Give the position of every Plasmodium parasite visible.
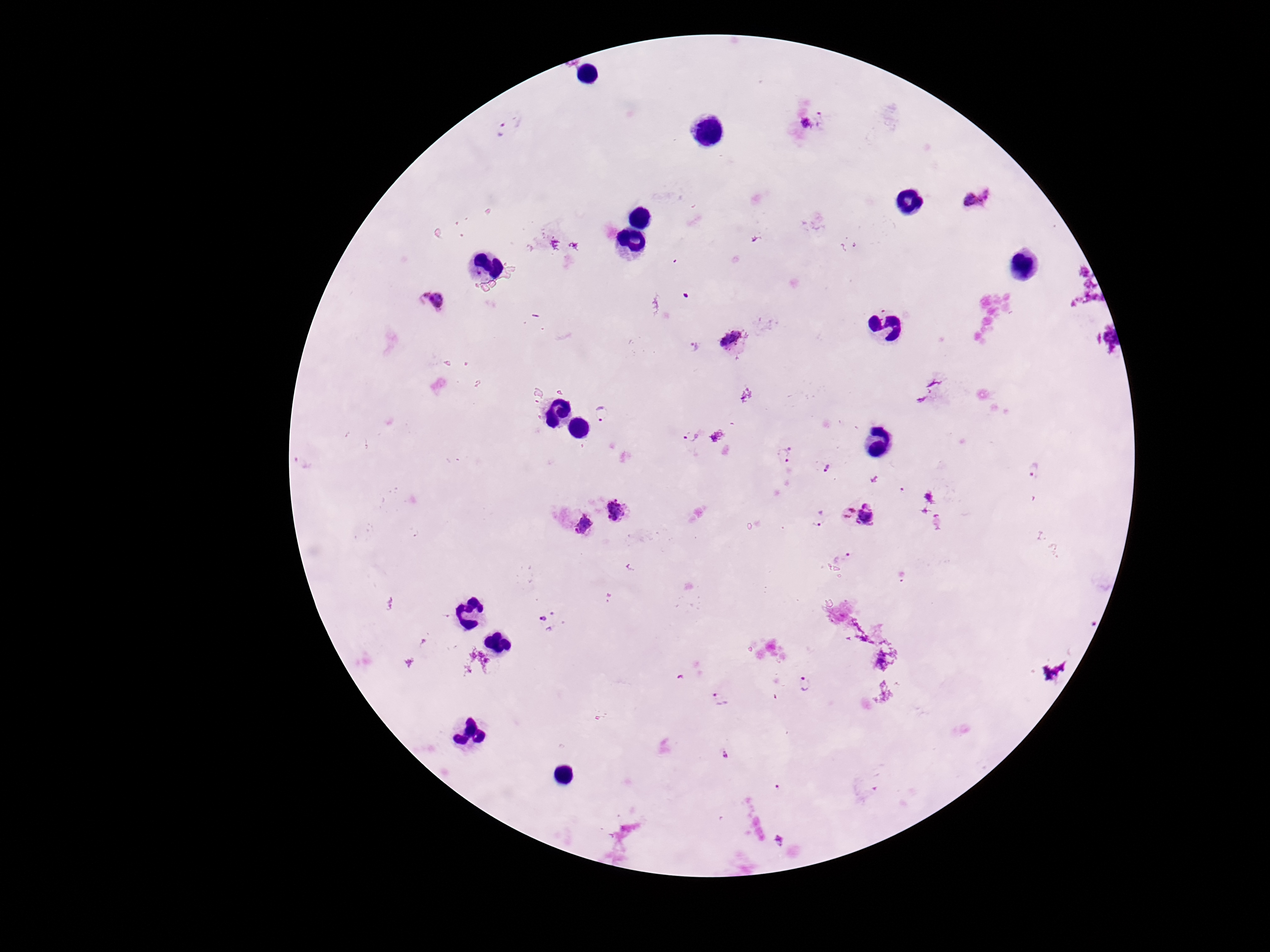
Approximate centers as [x, y] in pixels.
Plasmodium parasites: [812, 123], [504, 130], [979, 199], [432, 302], [733, 339], [693, 347], [603, 415], [693, 437], [785, 454], [825, 467], [1033, 472], [616, 511], [864, 515], [819, 521], [579, 526], [842, 558], [547, 621], [804, 687], [718, 697], [725, 755].

preparation = thick blood smear
magnification = 100x
stain = Giemsa
capture = smartphone camera through the microscope eyepiece
field of view = single
patient malaria status = infected
image size = 1270×952 pixels